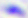

Toxoplasma gondii is seen. Micrograph. 400x magnification.